Report the malaria status of this cell.
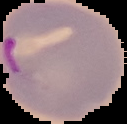
Parasitized.

preparation: thin blood smear
image_size: 127×124 pixels
image_type: segmented cell region on a black background